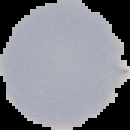

Summary:
  - Malaria status: uninfected
  - Preparation: thin blood film
  - Image size: 130×130 pixels
  - Image type: cell region segmented out of the field of view; surrounding area masked to black